Classify this cell by malaria status.
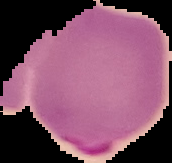

Parasitized.

Summary:
  - Image size: 172×163 pixels
  - Image type: cell region segmented out of the field of view; surrounding area masked to black
  - Preparation: thin blood smear